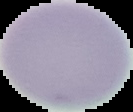
image size = 133×112 pixels
preparation = thin blood film
image type = segmented cell region on a black background
result = negative for malaria parasites